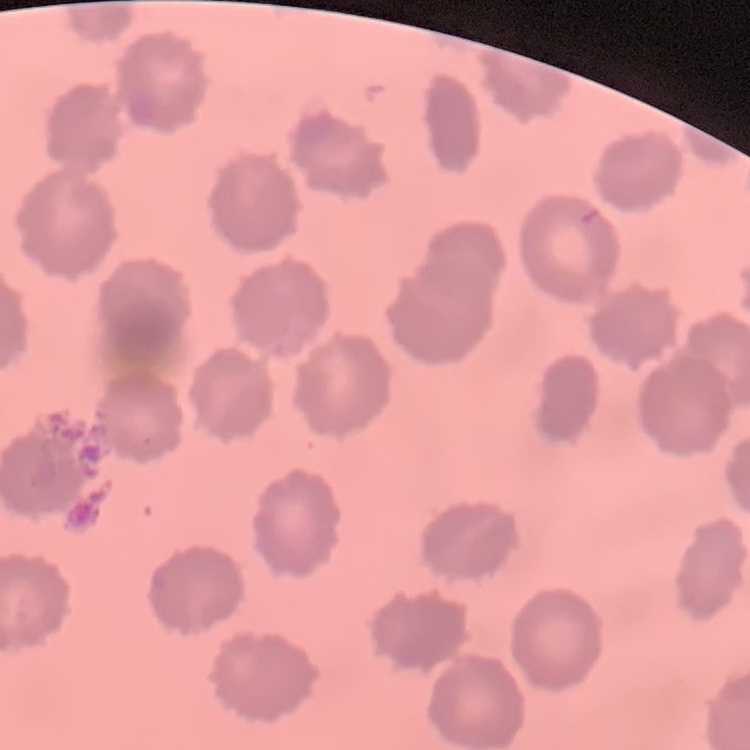
The erythrocytes exhibit no rouleaux formation. Square crop of a larger photomicrograph. Field's or Giemsa stain. Thin blood film.